Locate and identify every blood parasite.
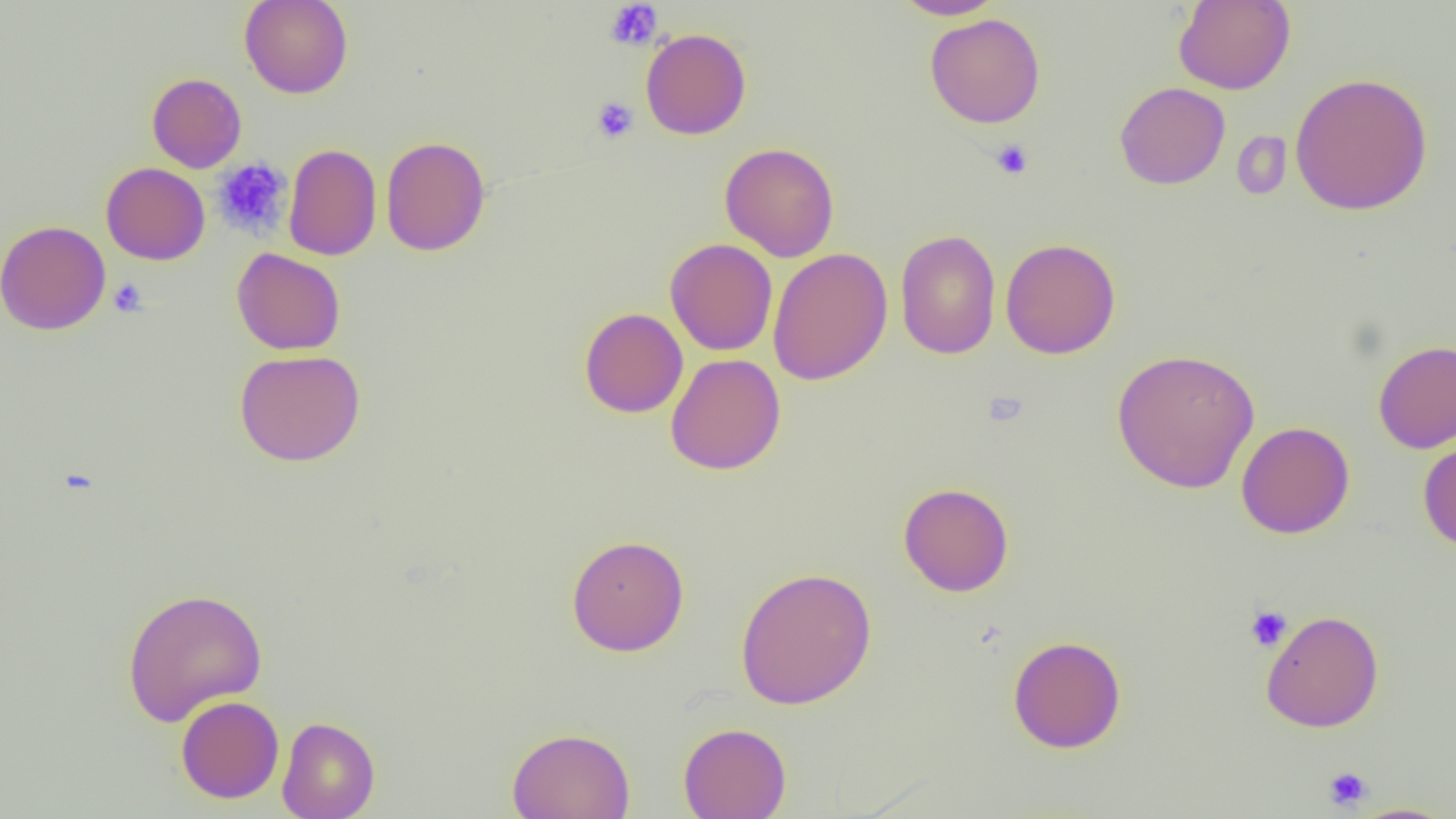

No blood parasites observed.

Summary:
  - Coordinate format: approximate bounding boxes as [x1, y1, x2, y2] in pixels
  - Uninfected red blood cell locations: [239, 0, 354, 99], [892, 0, 1005, 19], [1173, 1, 1295, 94], [924, 13, 1045, 128], [640, 28, 751, 140], [1289, 72, 1433, 215], [146, 73, 247, 173], [1115, 81, 1230, 189], [1232, 131, 1292, 201], [380, 136, 491, 256], [719, 142, 839, 261], [283, 143, 382, 261], [100, 162, 211, 265], [0, 220, 111, 336], [895, 229, 1001, 359], [665, 238, 778, 355], [1000, 238, 1120, 359], [768, 247, 893, 386], [232, 248, 345, 355], [579, 307, 688, 418], [1373, 339, 1456, 453], [1111, 348, 1260, 494], [234, 349, 366, 466], [665, 353, 786, 475], [1236, 421, 1355, 539], [1417, 435, 1456, 553], [898, 482, 1014, 596], [566, 534, 689, 655], [735, 566, 877, 710], [121, 586, 268, 726], [1260, 609, 1384, 732], [1008, 635, 1126, 753], [175, 695, 284, 804], [277, 716, 380, 819], [678, 722, 792, 819], [507, 727, 635, 819], [1345, 803, 1456, 819]
  - Platelet locations: [605, 1, 663, 51], [591, 97, 639, 143], [989, 139, 1034, 179], [212, 157, 293, 239], [108, 278, 147, 318], [1244, 605, 1292, 652], [1322, 766, 1373, 810]
  - Slide-level diagnosis: negative for blood parasites
  - Modality: optical microscopy
  - Magnification: 1000x
  - Preparation: thin blood smear
  - Field of view: single
  - Image size: 1456×819 pixels